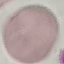
{
  "malaria_status": "uninfected",
  "preparation": "thin blood film",
  "image_type": "automatically extracted cell patch, resized to 64 × 64 pixels",
  "stain": "Giemsa",
  "capture": "smartphone through the microscope eyepiece"
}